Assess the morphology of the red blood cells.
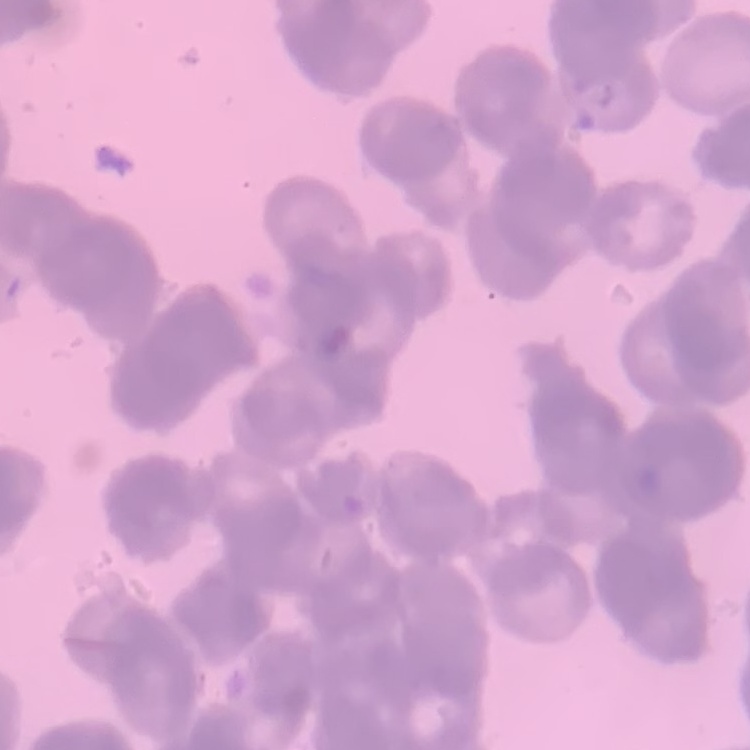

They show rouleaux formation.

stain = Field's or Giemsa
image type = one tile cut from a larger photomicrograph
preparation = thin blood smear